Outline each blood parasite and name the species.
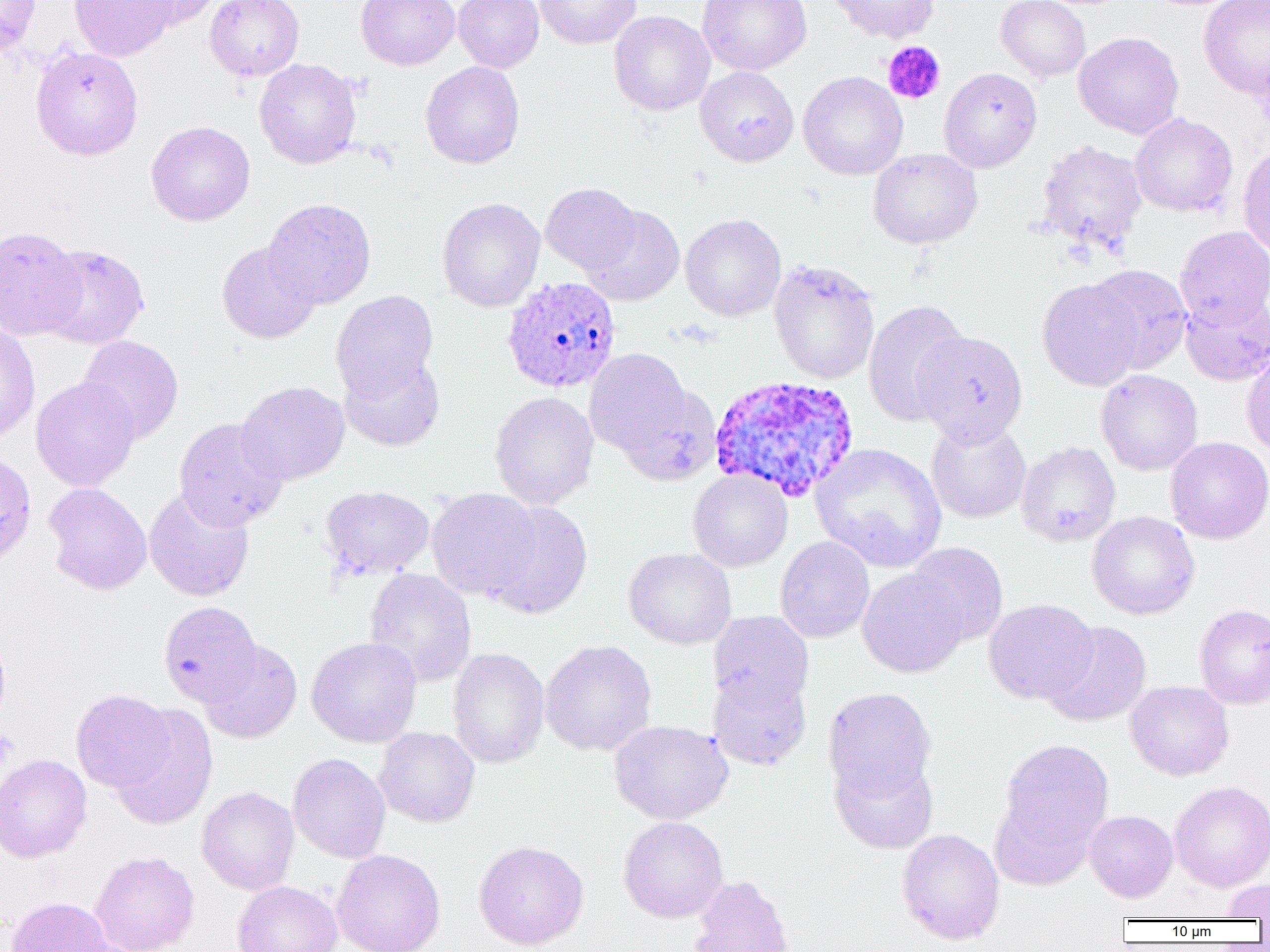
Approximate bounding boxes as named x1/y1/x2/y2 corners in pixels.
Plasmodium ovale-infected red blood cells: (x1=501, y1=276, x2=621, y2=393), (x1=709, y1=374, x2=860, y2=503).
No Plasmodium falciparum, Plasmodium malariae, Plasmodium vivax, Babesia divergens, or Trypanosoma brucei observed.

slide-level diagnosis = Plasmodium ovale
modality = optical microscopy
preparation = thin blood smear
magnification = 1000x
field of view = single
uninfected red blood cell locations = approximate bounding boxes as named x1/y1/x2/y2 corners in pixels: (x1=0, y1=0, x2=42, y2=57), (x1=69, y1=0, x2=177, y2=62), (x1=126, y1=0, x2=223, y2=29), (x1=205, y1=0, x2=304, y2=81), (x1=356, y1=0, x2=460, y2=70), (x1=453, y1=0, x2=544, y2=73), (x1=535, y1=0, x2=641, y2=49), (x1=696, y1=0, x2=812, y2=76), (x1=826, y1=0, x2=939, y2=43), (x1=996, y1=0, x2=1091, y2=82), (x1=1198, y1=0, x2=1270, y2=99), (x1=609, y1=11, x2=715, y2=116), (x1=1074, y1=32, x2=1184, y2=139), (x1=30, y1=46, x2=144, y2=160), (x1=254, y1=59, x2=362, y2=169), (x1=420, y1=61, x2=524, y2=169), (x1=695, y1=66, x2=799, y2=166), (x1=939, y1=67, x2=1042, y2=173), (x1=798, y1=71, x2=907, y2=180), (x1=1130, y1=113, x2=1238, y2=217), (x1=146, y1=121, x2=255, y2=226), (x1=1036, y1=139, x2=1147, y2=255), (x1=1237, y1=145, x2=1270, y2=258), (x1=867, y1=148, x2=982, y2=249), (x1=540, y1=183, x2=641, y2=274), (x1=438, y1=198, x2=545, y2=312), (x1=263, y1=199, x2=376, y2=309), (x1=580, y1=205, x2=685, y2=306), (x1=680, y1=214, x2=786, y2=321), (x1=0, y1=225, x2=85, y2=341), (x1=1174, y1=225, x2=1270, y2=327), (x1=217, y1=241, x2=321, y2=344), (x1=39, y1=244, x2=149, y2=349), (x1=768, y1=259, x2=881, y2=384), (x1=1085, y1=264, x2=1193, y2=374), (x1=1037, y1=278, x2=1145, y2=391), (x1=331, y1=290, x2=439, y2=402), (x1=1180, y1=292, x2=1269, y2=386), (x1=863, y1=299, x2=970, y2=426), (x1=0, y1=322, x2=40, y2=445), (x1=913, y1=330, x2=1028, y2=445), (x1=78, y1=335, x2=184, y2=443), (x1=584, y1=348, x2=695, y2=459), (x1=1241, y1=350, x2=1270, y2=456), (x1=339, y1=353, x2=445, y2=452), (x1=1095, y1=369, x2=1203, y2=475), (x1=30, y1=377, x2=140, y2=491), (x1=236, y1=381, x2=350, y2=485), (x1=616, y1=384, x2=722, y2=486), (x1=490, y1=391, x2=599, y2=510), (x1=174, y1=418, x2=288, y2=531), (x1=926, y1=419, x2=1031, y2=523), (x1=1165, y1=437, x2=1270, y2=544), (x1=1016, y1=441, x2=1121, y2=546), (x1=811, y1=443, x2=946, y2=572), (x1=688, y1=470, x2=792, y2=572), (x1=43, y1=482, x2=152, y2=595), (x1=321, y1=485, x2=435, y2=580), (x1=144, y1=487, x2=254, y2=602), (x1=426, y1=488, x2=543, y2=601), (x1=483, y1=500, x2=594, y2=619), (x1=1087, y1=511, x2=1200, y2=620), (x1=774, y1=536, x2=875, y2=642), (x1=906, y1=542, x2=1008, y2=646), (x1=624, y1=547, x2=736, y2=649), (x1=365, y1=568, x2=476, y2=686), (x1=857, y1=568, x2=969, y2=677), (x1=983, y1=598, x2=1099, y2=704), (x1=159, y1=601, x2=262, y2=707), (x1=1194, y1=603, x2=1270, y2=709), (x1=708, y1=611, x2=814, y2=710), (x1=1041, y1=621, x2=1151, y2=727), (x1=0, y1=633, x2=11, y2=730), (x1=307, y1=636, x2=422, y2=748), (x1=540, y1=639, x2=657, y2=756), (x1=200, y1=640, x2=302, y2=743), (x1=448, y1=647, x2=550, y2=768), (x1=707, y1=668, x2=811, y2=770), (x1=1124, y1=681, x2=1234, y2=780), (x1=823, y1=688, x2=936, y2=801), (x1=71, y1=689, x2=174, y2=792), (x1=109, y1=704, x2=218, y2=830), (x1=609, y1=719, x2=733, y2=824), (x1=374, y1=727, x2=480, y2=827), (x1=999, y1=740, x2=1114, y2=851), (x1=0, y1=753, x2=92, y2=863), (x1=288, y1=753, x2=391, y2=863), (x1=830, y1=753, x2=938, y2=853), (x1=1169, y1=781, x2=1270, y2=892), (x1=196, y1=787, x2=299, y2=895), (x1=990, y1=795, x2=1094, y2=890), (x1=1085, y1=810, x2=1178, y2=902), (x1=618, y1=816, x2=728, y2=923), (x1=897, y1=829, x2=1004, y2=945), (x1=474, y1=840, x2=589, y2=950), (x1=332, y1=849, x2=445, y2=952), (x1=89, y1=850, x2=199, y2=952), (x1=689, y1=875, x2=793, y2=952), (x1=1220, y1=878, x2=1270, y2=919), (x1=232, y1=880, x2=342, y2=952), (x1=6, y1=897, x2=116, y2=952)
platelet locations = approximate bounding boxes as named x1/y1/x2/y2 corners in pixels: (x1=882, y1=41, x2=945, y2=105), (x1=0, y1=730, x2=18, y2=766)
image size = 1270×952 pixels